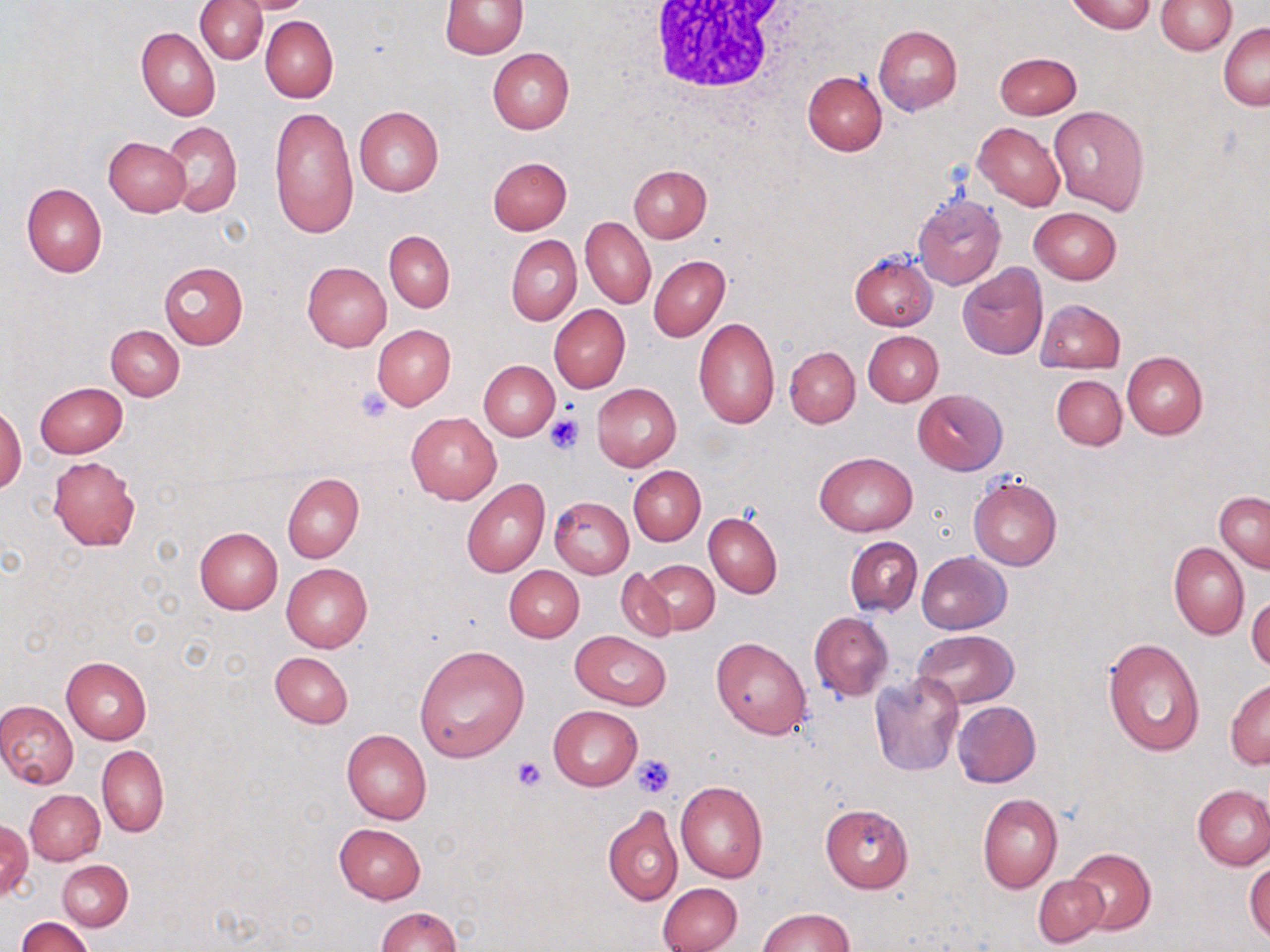

slide-level diagnosis = no evidence of blood parasites
magnification = 1000x
platelet locations = approximate bounding boxes as [x1, y1, x2, y2] in pixels: [353, 385, 394, 424], [544, 414, 584, 455], [631, 754, 675, 797], [510, 756, 546, 791]
uninfected red blood cell locations = approximate bounding boxes as [x1, y1, x2, y2] in pixels: [197, 0, 267, 64], [235, 0, 318, 14], [1069, 0, 1155, 34], [1156, 0, 1237, 54], [441, 1, 527, 58], [259, 15, 337, 103], [1219, 23, 1270, 109], [873, 24, 961, 115], [136, 27, 220, 121], [487, 48, 574, 134], [992, 51, 1082, 119], [802, 71, 886, 156], [1048, 105, 1149, 213], [354, 106, 444, 196], [269, 107, 358, 239], [162, 121, 242, 218], [974, 121, 1064, 210], [103, 137, 189, 217], [487, 156, 572, 234], [629, 164, 712, 242], [22, 182, 107, 277], [910, 192, 1006, 291], [1028, 207, 1122, 284], [581, 216, 655, 309], [385, 230, 454, 313], [506, 235, 582, 325], [849, 251, 937, 330], [648, 255, 730, 342], [159, 261, 248, 349], [302, 261, 391, 351], [958, 264, 1049, 360], [1036, 298, 1125, 373], [550, 305, 631, 393], [693, 317, 780, 429], [107, 324, 185, 400], [372, 324, 455, 410], [863, 330, 943, 406], [785, 346, 859, 427], [1121, 351, 1207, 439], [479, 360, 559, 440], [1051, 374, 1126, 450], [35, 381, 127, 457], [591, 383, 681, 470], [913, 389, 1007, 474], [0, 405, 24, 494], [406, 412, 502, 504], [813, 453, 918, 536], [48, 457, 139, 551], [628, 465, 706, 546], [281, 473, 363, 563], [968, 476, 1062, 570], [462, 478, 549, 577], [1214, 491, 1270, 574], [550, 497, 634, 578], [703, 511, 783, 598], [194, 527, 283, 614], [845, 537, 923, 616], [1169, 541, 1249, 639], [915, 551, 1011, 634], [638, 560, 719, 636], [281, 562, 373, 652], [504, 566, 584, 642], [615, 568, 677, 643], [1247, 593, 1270, 673], [809, 611, 893, 701], [930, 621, 1025, 771], [912, 629, 1019, 707], [570, 631, 670, 710], [711, 637, 812, 738], [1102, 637, 1204, 757], [414, 644, 528, 763], [270, 651, 354, 728], [61, 656, 152, 744], [869, 674, 963, 777], [1226, 679, 1270, 768], [0, 700, 80, 789], [952, 700, 1040, 787], [548, 705, 643, 790], [342, 729, 430, 825], [97, 745, 168, 837], [675, 779, 768, 883], [1192, 786, 1270, 869], [26, 789, 105, 865], [603, 794, 763, 894], [977, 794, 1062, 893], [820, 803, 913, 893], [603, 805, 683, 905], [1, 820, 32, 903], [333, 822, 426, 904], [1067, 847, 1155, 935], [1245, 858, 1270, 942], [56, 860, 132, 931], [1033, 875, 1108, 947], [658, 882, 742, 952], [375, 906, 463, 951], [757, 907, 853, 951], [17, 916, 93, 951]
preparation = thin blood film
modality = light microscopy
field of view = one of a larger specimen
white blood cell locations = approximate bounding boxes as [x1, y1, x2, y2] in pixels: [640, 2, 809, 100]
image size = 1270×952 pixels
stain = May-Grünwald-Giemsa